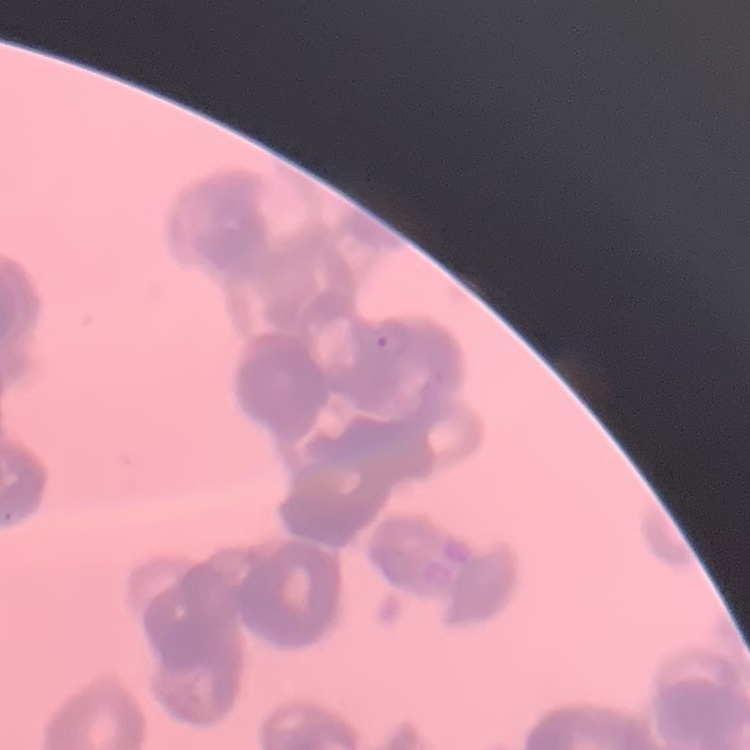
Summary:
  - Red blood cell morphology: rouleaux formation
  - Preparation: thin blood film
  - Image type: one tile cut from a larger photomicrograph
  - Stain: Field's or Giemsa